Identify the parasite.
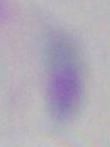

Toxoplasma gondii.

Captured at 1000x magnification. Photomicrograph.